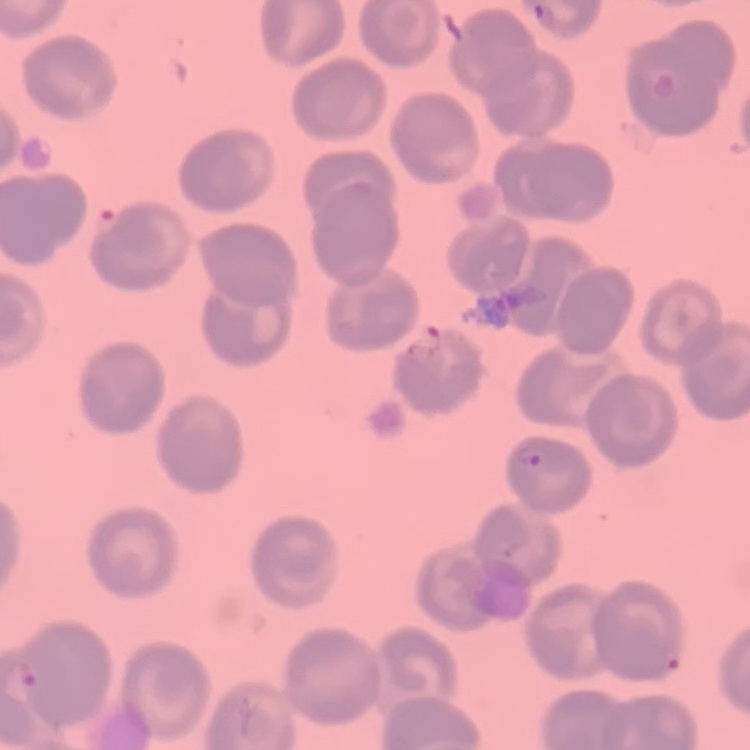

The erythrocytes show no rouleaux formation. Stained with either Field's or Giemsa. Thin blood film. One tile cut from a larger photomicrograph.